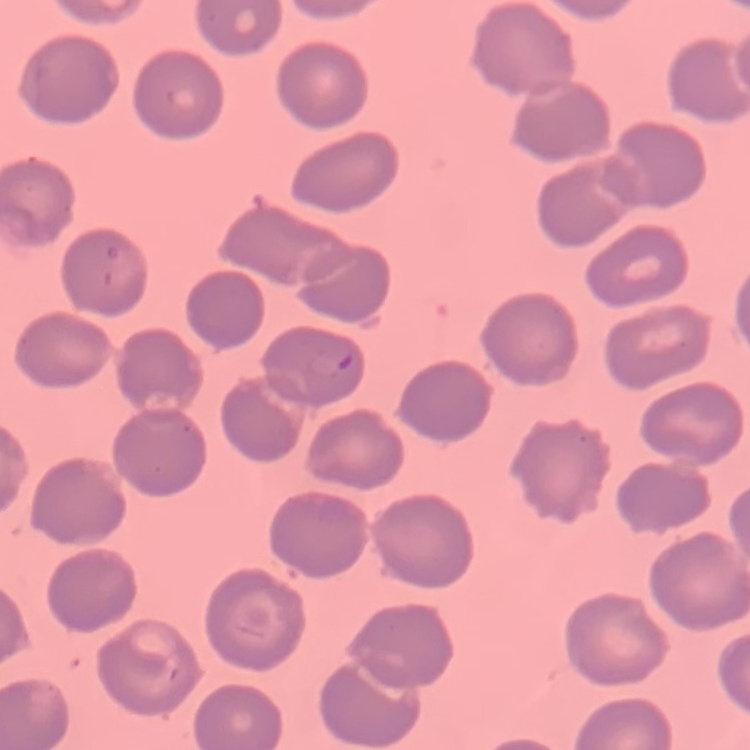
Summary:
  - Red blood cell morphology: no rouleaux formation
  - Preparation: thin peripheral smear
  - Image type: one tile cut from a larger photomicrograph
  - Stain: Field's or Giemsa